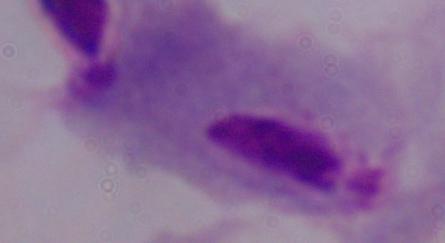

identification = trichomonad
modality = photomicrograph
magnification = 1000x